Locate every uninfected red blood cell.
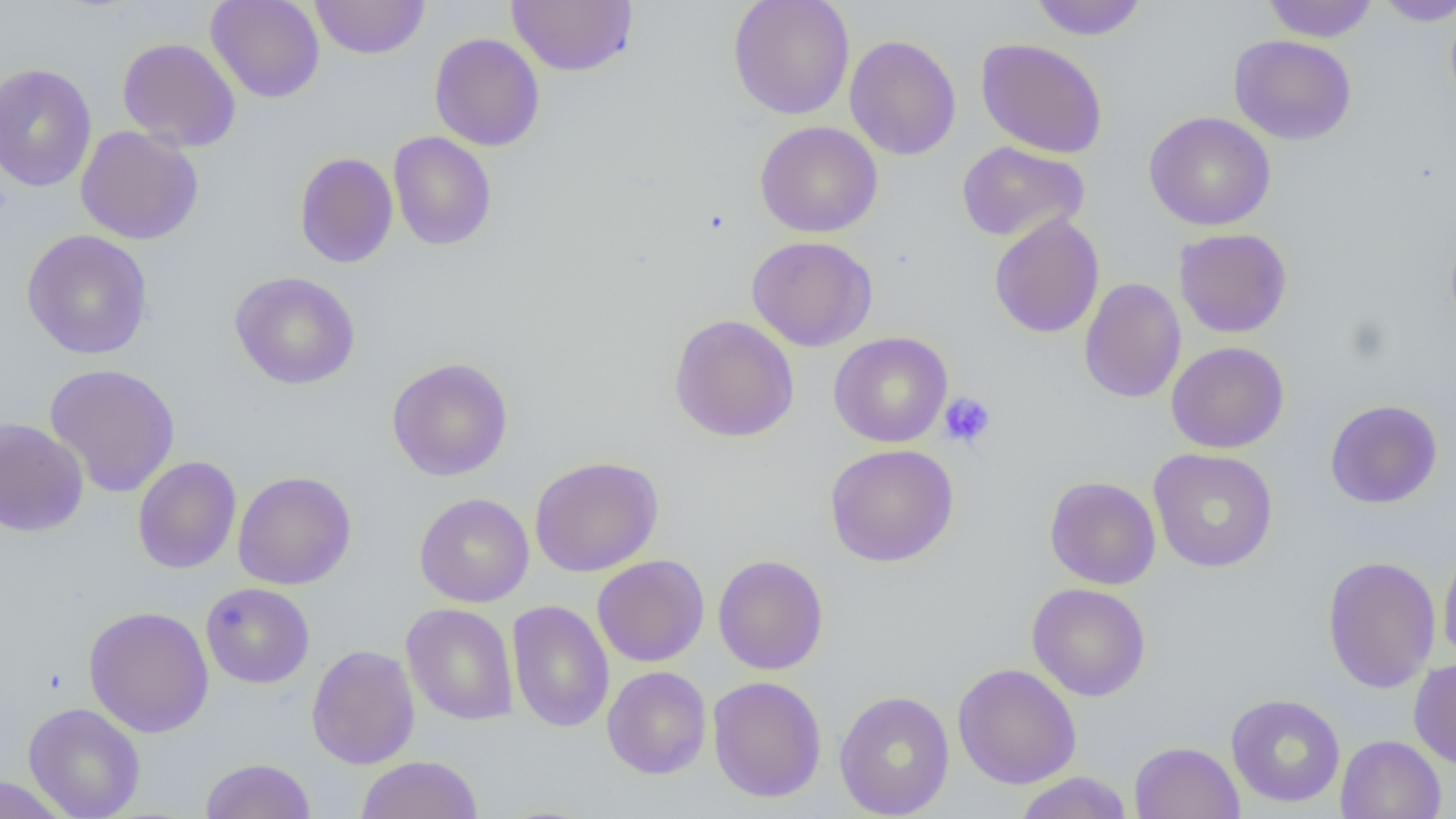

Approximate bounding boxes as named x1/y1/x2/y2 corners in pixels.
Uninfected red blood cells: (x1=206, y1=0, x2=325, y2=103), (x1=309, y1=0, x2=431, y2=59), (x1=727, y1=0, x2=855, y2=120), (x1=1029, y1=0, x2=1148, y2=41), (x1=1262, y1=0, x2=1379, y2=42), (x1=1373, y1=0, x2=1455, y2=26), (x1=506, y1=1, x2=637, y2=76), (x1=429, y1=33, x2=545, y2=151), (x1=844, y1=34, x2=962, y2=160), (x1=1228, y1=34, x2=1357, y2=145), (x1=117, y1=37, x2=241, y2=152), (x1=976, y1=38, x2=1108, y2=158), (x1=0, y1=62, x2=98, y2=192), (x1=1144, y1=110, x2=1276, y2=231), (x1=755, y1=121, x2=883, y2=238), (x1=75, y1=126, x2=204, y2=245), (x1=388, y1=131, x2=497, y2=250), (x1=957, y1=140, x2=1089, y2=243), (x1=294, y1=152, x2=398, y2=268), (x1=989, y1=212, x2=1105, y2=338), (x1=1445, y1=227, x2=1456, y2=341), (x1=1174, y1=228, x2=1293, y2=338), (x1=21, y1=229, x2=154, y2=360), (x1=747, y1=235, x2=878, y2=352), (x1=229, y1=270, x2=361, y2=390), (x1=1079, y1=278, x2=1186, y2=403), (x1=669, y1=314, x2=800, y2=442), (x1=829, y1=331, x2=953, y2=448), (x1=1166, y1=341, x2=1290, y2=454), (x1=386, y1=357, x2=514, y2=481), (x1=44, y1=363, x2=181, y2=498), (x1=1325, y1=399, x2=1443, y2=509), (x1=0, y1=418, x2=89, y2=537), (x1=824, y1=444, x2=959, y2=567), (x1=1148, y1=448, x2=1278, y2=573), (x1=132, y1=456, x2=241, y2=574), (x1=529, y1=456, x2=663, y2=577), (x1=232, y1=470, x2=357, y2=590), (x1=1045, y1=476, x2=1161, y2=590), (x1=414, y1=492, x2=534, y2=608), (x1=1438, y1=536, x2=1456, y2=669), (x1=713, y1=554, x2=829, y2=675), (x1=592, y1=555, x2=709, y2=667), (x1=1321, y1=555, x2=1441, y2=694), (x1=201, y1=582, x2=315, y2=688), (x1=1027, y1=582, x2=1151, y2=702), (x1=506, y1=599, x2=614, y2=733), (x1=401, y1=603, x2=519, y2=726), (x1=83, y1=605, x2=214, y2=738), (x1=306, y1=644, x2=420, y2=769), (x1=1408, y1=658, x2=1456, y2=769), (x1=953, y1=662, x2=1082, y2=790), (x1=601, y1=665, x2=711, y2=779), (x1=707, y1=675, x2=827, y2=803), (x1=834, y1=690, x2=955, y2=818), (x1=1225, y1=693, x2=1346, y2=808), (x1=23, y1=701, x2=146, y2=819), (x1=1335, y1=734, x2=1446, y2=819), (x1=1129, y1=740, x2=1245, y2=819), (x1=355, y1=755, x2=483, y2=818), (x1=200, y1=757, x2=317, y2=819), (x1=1013, y1=772, x2=1134, y2=819), (x1=0, y1=774, x2=72, y2=818).

Platelet locations: (x1=938, y1=392, x2=996, y2=449). Slide-level diagnosis: no evidence of blood parasites. Single field of view. Thin blood smear. Image is 1456×819 pixels. Captured at 1000x magnification. Light microscopy.